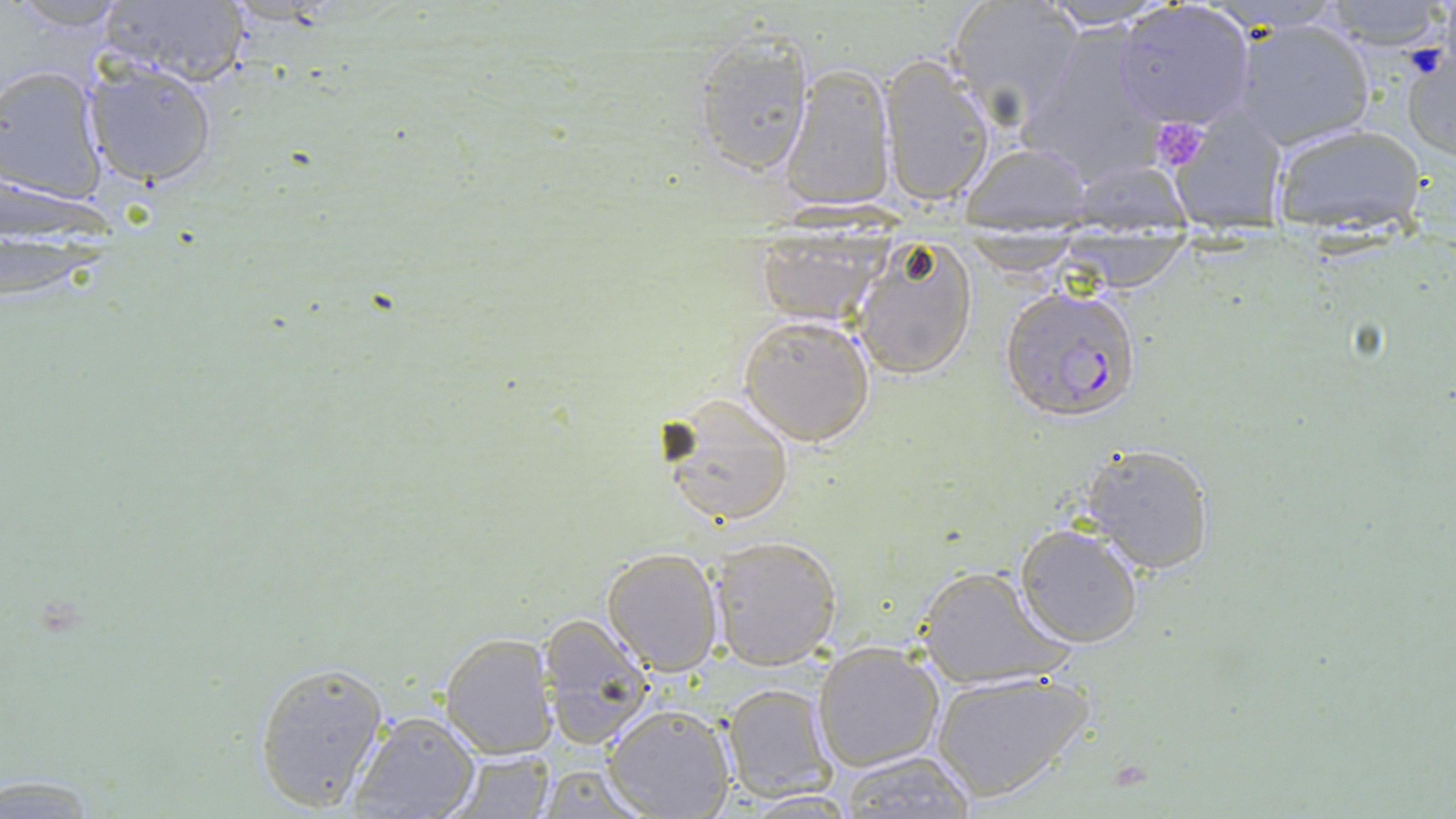

Summary:
  - Coordinate format: approximate bounding boxes as named x1/y1/x2/y2 corners in pixels
  - Uninfected red blood cell locations (subset): (x1=944, y1=0, x2=1082, y2=126), (x1=7, y1=1, x2=131, y2=31), (x1=1034, y1=1, x2=1181, y2=31), (x1=1318, y1=1, x2=1450, y2=49), (x1=92, y1=3, x2=253, y2=86), (x1=1115, y1=4, x2=1254, y2=129), (x1=1232, y1=16, x2=1376, y2=151), (x1=1020, y1=21, x2=1165, y2=181), (x1=689, y1=32, x2=816, y2=177), (x1=1400, y1=41, x2=1456, y2=162), (x1=876, y1=55, x2=994, y2=207), (x1=81, y1=60, x2=221, y2=187), (x1=779, y1=63, x2=896, y2=211), (x1=1, y1=64, x2=110, y2=202), (x1=1167, y1=106, x2=1287, y2=224), (x1=1270, y1=122, x2=1428, y2=226), (x1=957, y1=139, x2=1095, y2=228), (x1=4, y1=180, x2=116, y2=235), (x1=750, y1=231, x2=894, y2=326), (x1=1051, y1=234, x2=1196, y2=293), (x1=956, y1=235, x2=1085, y2=276), (x1=849, y1=237, x2=978, y2=380), (x1=737, y1=313, x2=878, y2=447), (x1=658, y1=392, x2=796, y2=531), (x1=1079, y1=443, x2=1219, y2=574), (x1=1014, y1=524, x2=1144, y2=649), (x1=708, y1=535, x2=842, y2=669), (x1=601, y1=547, x2=722, y2=674), (x1=914, y1=563, x2=1070, y2=691), (x1=539, y1=615, x2=659, y2=743), (x1=440, y1=634, x2=556, y2=758), (x1=813, y1=641, x2=945, y2=772), (x1=254, y1=659, x2=388, y2=812), (x1=931, y1=668, x2=1093, y2=803), (x1=722, y1=683, x2=835, y2=800), (x1=602, y1=705, x2=736, y2=819), (x1=349, y1=711, x2=479, y2=818), (x1=444, y1=746, x2=559, y2=818), (x1=838, y1=749, x2=976, y2=818), (x1=532, y1=763, x2=656, y2=816)
  - Platelet locations: (x1=1150, y1=118, x2=1209, y2=171)
  - Slide-level diagnosis: Plasmodium falciparum
  - Field of view: one of a larger specimen
  - Stain: May-Grünwald-Giemsa
  - Preparation: thin blood smear
  - Image size: 1456×819 pixels
  - Modality: optical microscopy
  - Magnification: 1000x